Report the malaria status of this cell.
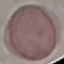
It is uninfected.

Acquired by smartphone through the microscope eyepiece. Thin smear of blood. Automatically extracted cell patch, resized to 64 × 64 pixels. Giemsa-stained preparation.